Point out each malaria parasite.
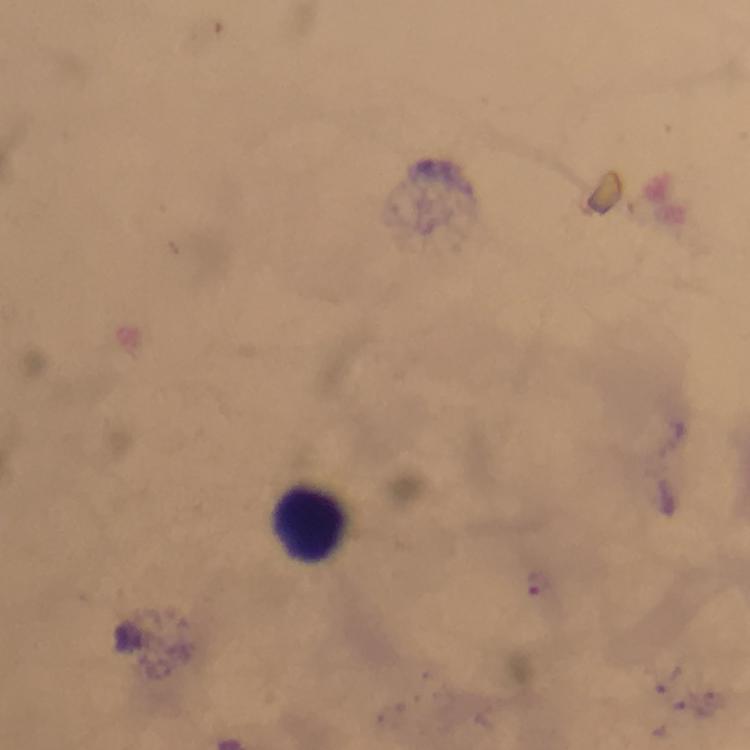

Approximate centers as [x, y] in pixels.
Malaria parasites: [539, 580].

Leukocyte locations: [312, 523]. Thick blood smear. From a malaria diagnostic workup. Image is 750×750 pixels. Photographed through the microscope with a smartphone camera. Giemsa-stained preparation. Cropped region of a single field of view. Immersion oil applied. At 100x magnification.